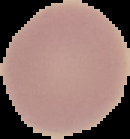 From a thin blood smear. The area outside the segmented cell region is set to black. Malaria status: uninfected. Image is 130×139 pixels.